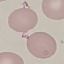 Malaria status: uninfected. Giemsa-stained preparation. Cell patch, automatically extracted from a larger field of view and resized to 64 × 64 pixels. Thin smear of blood. Photographed with a smartphone camera at the microscope eyepiece.